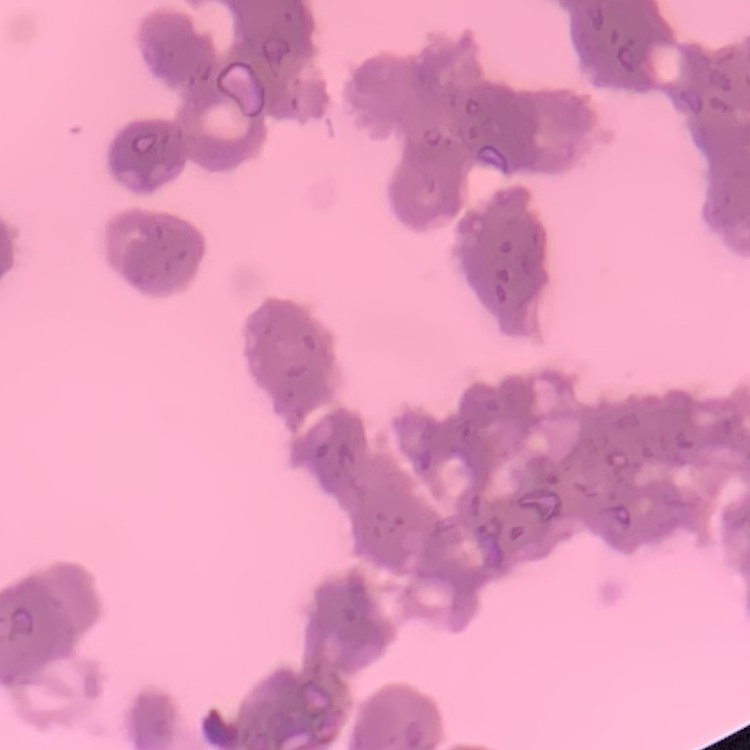
erythrocyte_morphology: rouleaux formation
stain: Field's or Giemsa
preparation: thin peripheral smear
image_type: one tile cut from a larger photomicrograph